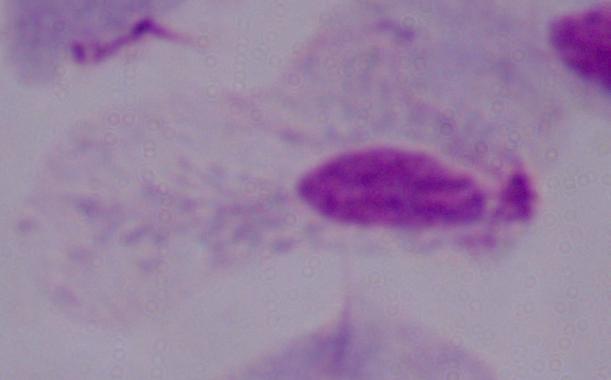

modality: photomicrograph
identification: trichomonad
magnification: 1000x